Describe the morphology of the erythrocytes.
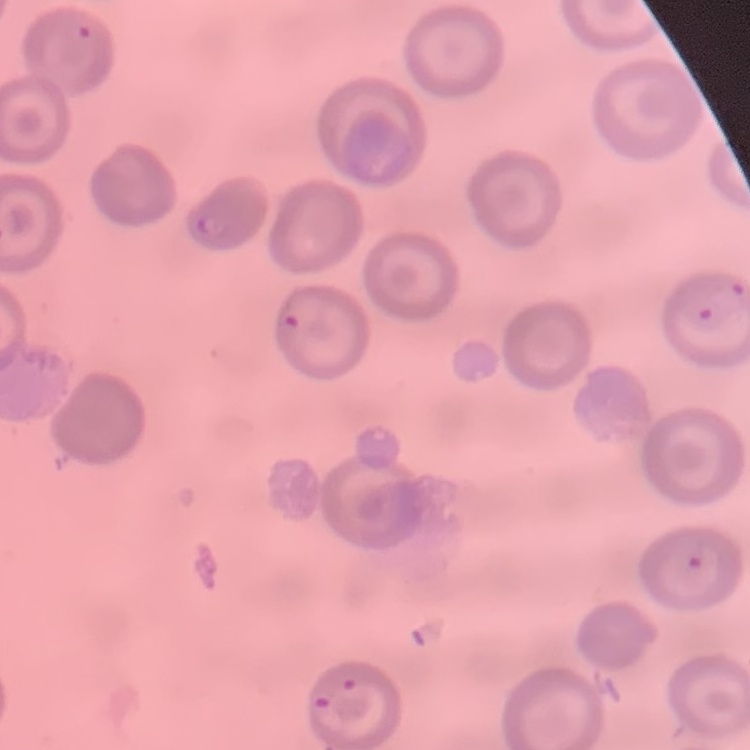
They show no rouleaux formation.

Summary:
  - Preparation: thin blood film
  - Image type: square crop of a larger photomicrograph
  - Stain: Field's or Giemsa